Outline each blood parasite and name the species.
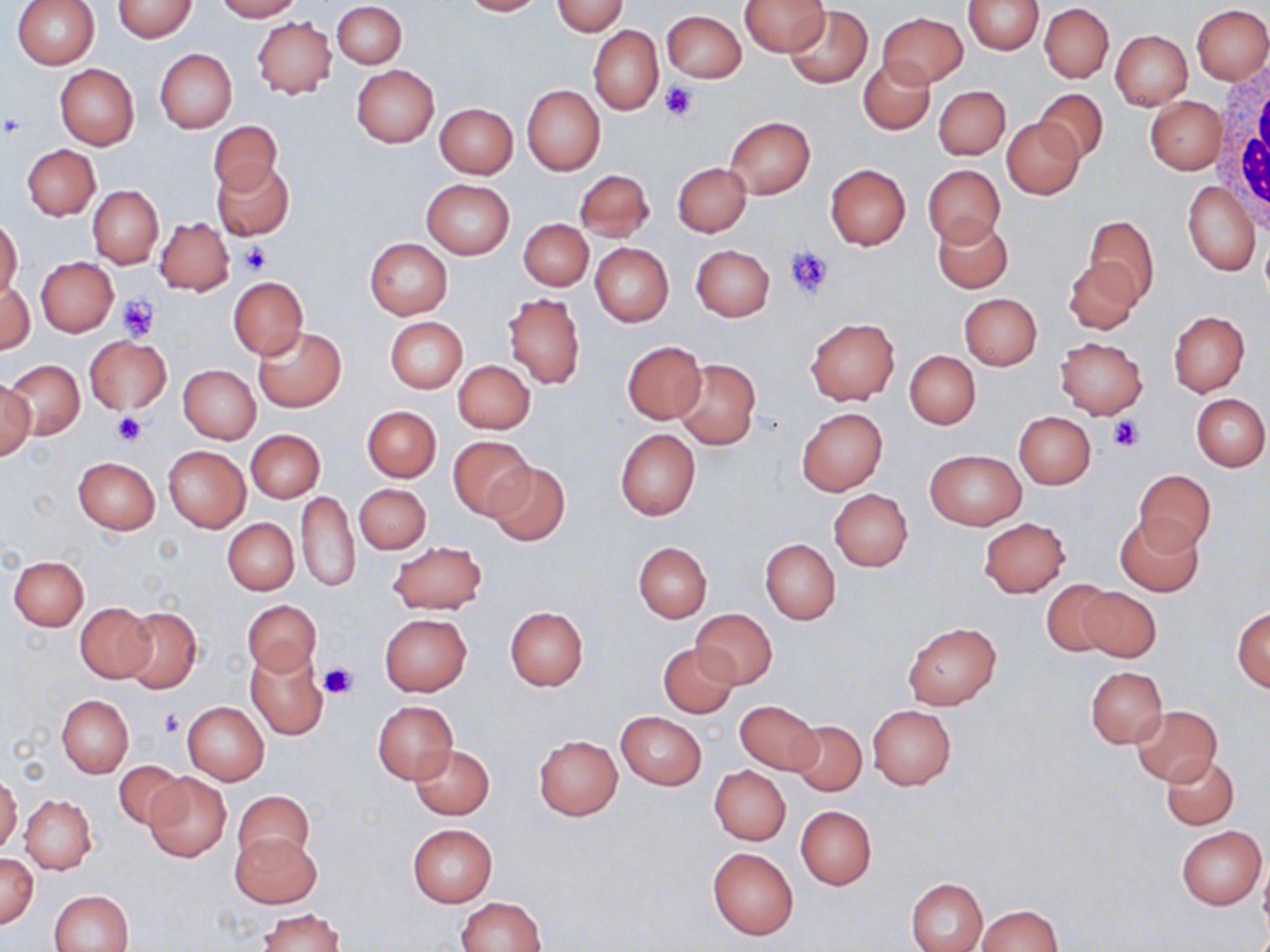
No blood parasites seen.

{
  "slide_level_diagnosis": "negative for blood parasites",
  "stain": "May-Grünwald-Giemsa",
  "image_size": "1270×952 pixels",
  "modality": "light microscopy",
  "field_of_view": "one of a larger specimen",
  "magnification": "1000x",
  "platelet_locations": "approximate bounding boxes as (x1,y1)-(x2,y2) corner pairs in pixels: (659,82)-(700,123), (1,112)-(26,138), (236,242)-(271,275), (785,246)-(834,300), (117,296)-(159,341), (112,411)-(148,448), (1106,415)-(1146,453), (319,660)-(359,698), (159,709)-(185,737)",
  "white_blood_cell_locations": "approximate bounding boxes as (x1,y1)-(x2,y2) corner pairs in pixels: (1212,68)-(1270,242)",
  "preparation": "thin blood film",
  "uninfected_red_blood_cell_locations": "approximate bounding boxes as (x1,y1)-(x2,y2) corner pairs in pixels: (12,0)-(100,68), (113,0)-(197,42), (214,0)-(300,21), (459,0)-(543,16), (740,0)-(829,56), (963,0)-(1044,54), (333,1)-(406,68), (551,1)-(628,36), (1039,4)-(1113,82), (1192,4)-(1270,85), (784,5)-(872,90), (662,10)-(746,82), (878,12)-(967,88), (250,17)-(336,99), (589,24)-(663,115), (1109,29)-(1192,110), (155,49)-(236,132), (857,57)-(933,134), (55,64)-(140,150), (351,64)-(440,147), (521,85)-(604,176), (933,86)-(1010,159), (1034,89)-(1108,163), (1146,97)-(1225,174), (435,103)-(517,178), (725,117)-(815,198), (1002,117)-(1084,198), (208,121)-(283,196), (22,144)-(100,220), (213,162)-(294,241), (672,162)-(751,237), (825,164)-(911,251), (923,164)-(1005,246), (574,169)-(654,242), (421,179)-(514,259), (1182,180)-(1259,275), (89,185)-(163,268), (933,214)-(1012,292), (1081,214)-(1159,306), (156,217)-(234,296), (0,218)-(22,298), (519,219)-(592,289), (364,238)-(452,319), (590,242)-(673,326), (692,245)-(774,321), (35,257)-(117,336), (1064,257)-(1142,335), (229,277)-(308,358), (1,280)-(34,356), (503,293)-(584,389), (959,293)-(1043,370), (1169,310)-(1249,396), (384,317)-(468,392), (806,317)-(899,405), (252,326)-(345,412), (84,335)-(173,414), (1055,335)-(1148,419), (622,342)-(707,423), (904,350)-(981,429), (4,359)-(83,439), (672,359)-(761,450), (453,360)-(535,434), (178,364)-(260,443), (0,379)-(35,461), (1192,393)-(1269,472), (362,406)-(441,481), (796,407)-(888,494), (1013,411)-(1095,488), (615,429)-(700,520), (246,430)-(325,503), (448,435)-(534,519), (163,445)-(250,531), (925,450)-(1026,529), (72,457)-(159,535), (487,460)-(569,546), (1133,470)-(1215,553), (355,484)-(431,554), (829,488)-(913,572), (296,491)-(359,591), (1115,514)-(1204,597), (223,518)-(297,595), (978,518)-(1070,597), (760,538)-(840,624), (387,541)-(488,614), (633,541)-(712,622), (9,556)-(88,630), (1041,579)-(1117,656), (1076,586)-(1161,663), (242,599)-(321,676), (74,601)-(155,682), (505,606)-(588,691), (1232,606)-(1270,691), (120,607)-(201,694), (691,608)-(777,689), (379,613)-(472,695), (903,623)-(1001,708), (658,642)-(739,717), (246,650)-(328,739), (1085,667)-(1167,748), (57,694)-(133,777), (734,699)-(822,774), (182,701)-(269,784), (373,701)-(457,782), (868,705)-(955,790), (1131,705)-(1221,786), (617,711)-(707,790), (790,720)-(866,796), (533,734)-(622,820), (409,743)-(494,819), (1161,753)-(1238,829), (112,760)-(191,831), (710,766)-(791,844), (142,773)-(232,863), (0,774)-(21,853), (233,789)-(314,866), (21,794)-(97,874), (796,805)-(876,890), (407,823)-(498,906), (1175,825)-(1266,910), (230,833)-(320,908), (708,847)-(798,939), (0,854)-(39,928), (1259,859)-(1270,944), (906,877)-(987,952), (50,890)-(133,952), (456,897)-(547,951), (976,904)-(1065,951), (260,907)-(344,951)"
}